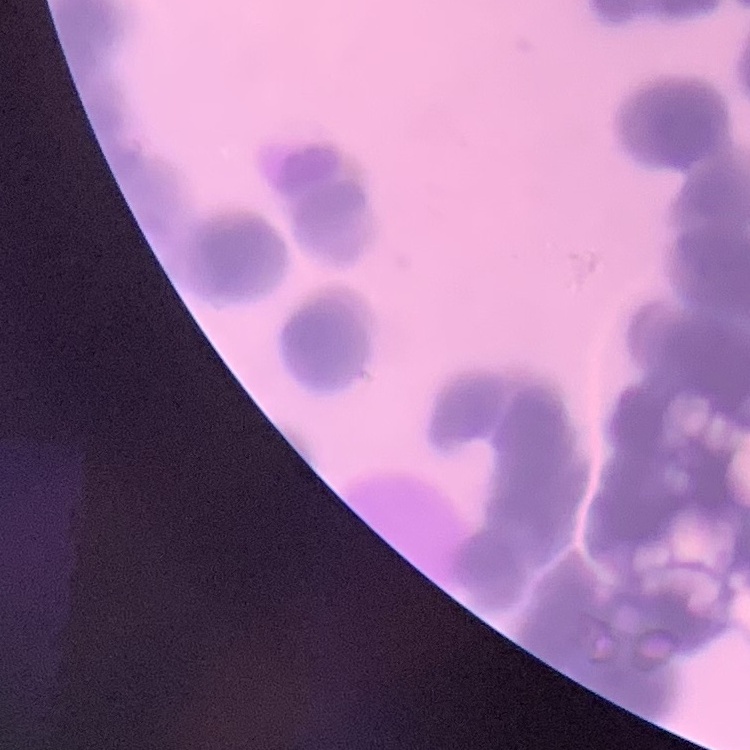

Summary:
  - Erythrocyte morphology: rouleaux formation
  - Image type: square crop of a larger photomicrograph
  - Preparation: thin blood smear
  - Stain: Field's or Giemsa